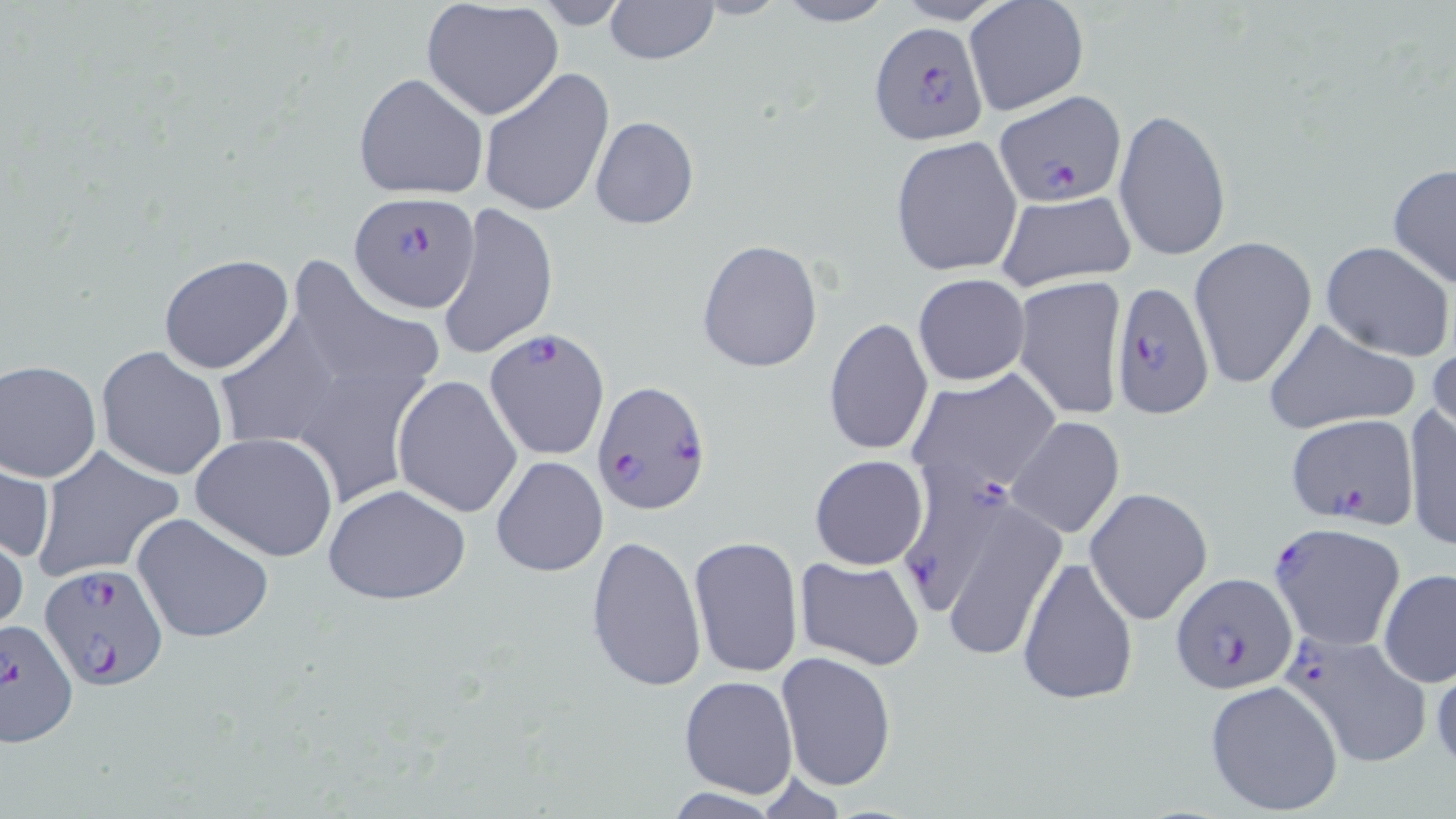

Approximate bounding boxes as [x1, y1, x2, y2] in pixels. Plasmodium falciparum-infected red blood cell locations: [867, 20, 990, 146], [993, 91, 1124, 208], [351, 191, 481, 313], [1106, 281, 1216, 417], [485, 327, 610, 461], [591, 378, 711, 513], [1287, 413, 1421, 535], [1269, 525, 1407, 649], [36, 562, 169, 689], [1167, 572, 1296, 694], [0, 619, 77, 752], [1284, 628, 1434, 769]. Uninfected red blood cell locations: [602, 0, 720, 66], [687, 0, 792, 20], [772, 0, 897, 26], [422, 2, 565, 121], [963, 2, 1089, 118], [479, 66, 615, 217], [354, 73, 489, 200], [1112, 105, 1232, 262], [590, 115, 698, 231], [890, 135, 1023, 276], [1386, 162, 1456, 291], [994, 190, 1138, 291], [438, 201, 559, 360], [1189, 235, 1318, 389], [696, 239, 824, 374], [1321, 241, 1454, 362], [157, 253, 294, 374], [290, 255, 446, 381], [912, 273, 1031, 387], [1011, 275, 1128, 421], [216, 312, 342, 445], [823, 317, 934, 457], [1261, 317, 1424, 436], [1427, 336, 1455, 445], [95, 344, 229, 480], [306, 357, 448, 504], [0, 358, 101, 483], [906, 369, 1060, 501], [393, 375, 522, 518], [1404, 403, 1455, 552], [1007, 417, 1125, 539], [189, 432, 339, 561], [31, 445, 186, 584], [490, 455, 608, 578], [809, 455, 929, 571], [0, 456, 53, 566], [323, 483, 474, 606], [1085, 487, 1214, 625], [927, 490, 1067, 665], [131, 512, 277, 644], [960, 513, 1119, 691], [0, 523, 27, 638], [584, 535, 706, 693], [688, 535, 804, 679], [1018, 555, 1140, 705], [794, 557, 926, 671], [1378, 568, 1455, 689], [775, 649, 897, 792], [1428, 651, 1456, 771], [678, 675, 799, 799], [1204, 679, 1345, 816]. Slide-level diagnosis: Plasmodium falciparum. Optical microscopy. Image is 1456×819 pixels. Thin blood film. May-Grünwald-Giemsa stain. Single field of view. Captured at 1000x magnification.